Locate every malaria parasite.
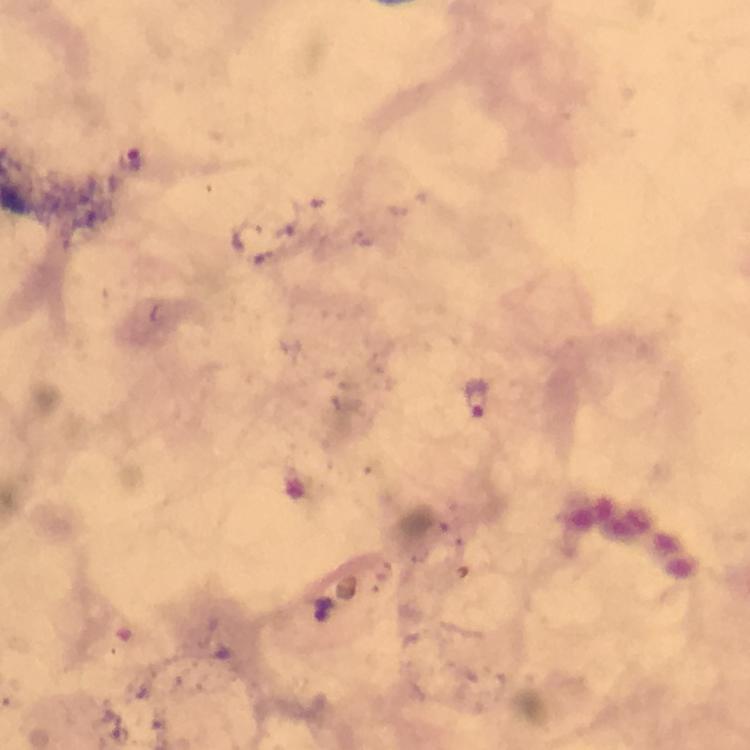

Approximate centers as {x, y} in pixels.
Malaria parasites: {133, 165}, {475, 398}.

Summary:
  - Image size: 750×750 pixels
  - Stain: Giemsa
  - Cropped from: one field of view
  - Context: from a malaria diagnostic workup
  - Magnification: 100x
  - Capture: smartphone photograph through a microscope
  - Immersion oil: used
  - Preparation: thick smear